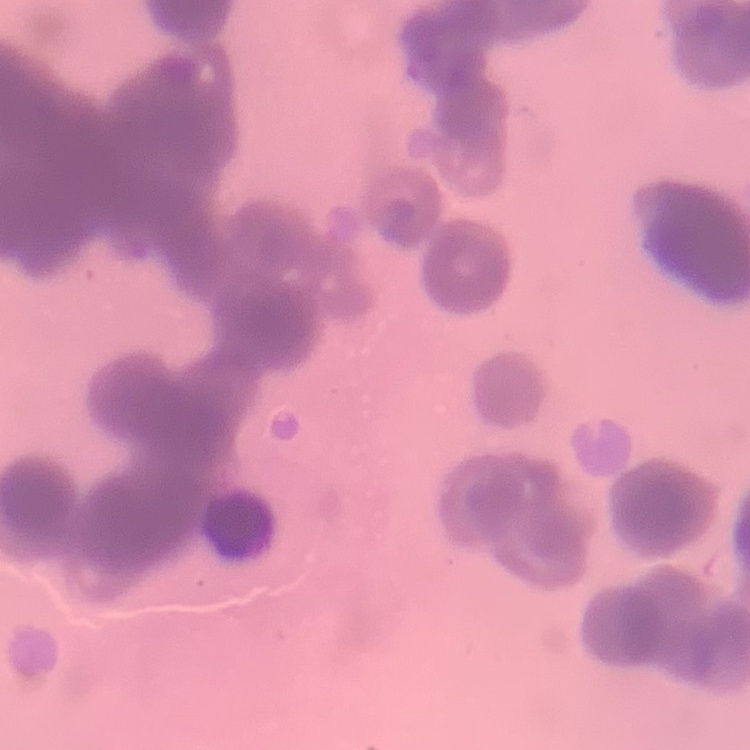
Summary:
  - Erythrocyte morphology: rouleaux formation
  - Preparation: thin peripheral smear
  - Image type: one tile cut from a larger photomicrograph
  - Stain: Field's or Giemsa